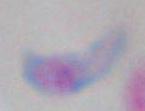

Summary:
  - Identification: Toxoplasma gondii
  - Magnification: 1000x
  - Modality: photomicrograph